Identify the preparation type.
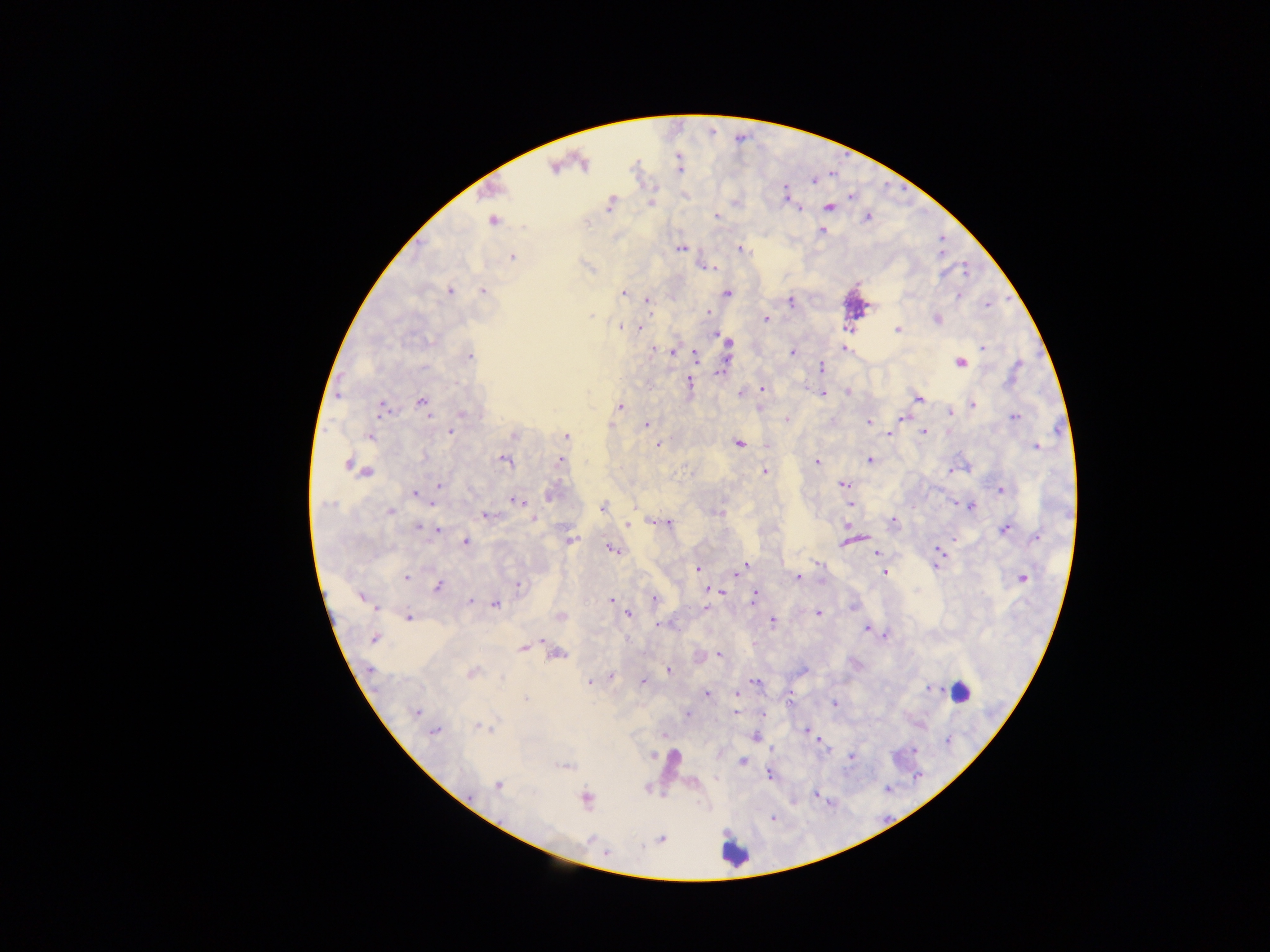
This is a thick smear.

Approximate centers as [x, y] in pixels. Plasmodium parasite locations: [554, 168], [813, 185], [784, 194], [614, 199], [651, 203], [828, 207], [796, 209], [718, 219], [492, 221], [587, 222], [821, 231], [739, 248], [680, 249], [512, 257], [716, 267], [964, 272], [945, 274], [940, 275], [482, 290], [450, 291], [623, 292], [727, 292], [958, 297], [647, 299], [790, 300], [988, 305], [708, 312], [592, 314], [938, 318], [765, 320], [622, 325], [640, 327], [897, 328], [845, 329], [721, 337], [729, 341], [845, 347], [983, 347], [657, 349], [792, 352], [694, 355], [471, 356], [960, 362], [821, 365], [1020, 365], [723, 368], [763, 388], [822, 392], [847, 392], [919, 399], [421, 403], [973, 403], [621, 406], [380, 412], [950, 412], [902, 416], [429, 417], [1014, 418], [868, 423], [609, 424], [646, 424], [450, 433], [891, 433], [925, 433], [512, 434], [369, 437], [565, 437], [739, 442], [658, 446], [1038, 446], [559, 458], [869, 460], [507, 462], [817, 462], [346, 465], [950, 470], [369, 471], [765, 471], [842, 485], [440, 486], [1003, 489], [416, 492], [512, 501], [517, 502], [636, 502], [849, 502], [972, 506], [602, 507], [391, 513], [484, 515], [533, 519], [670, 521], [894, 521], [627, 525], [418, 528], [440, 528], [1006, 528], [1037, 536], [861, 537], [956, 539], [465, 543], [571, 543], [844, 543], [613, 549], [940, 550], [876, 552], [746, 564], [819, 564], [696, 567], [941, 568], [736, 573], [884, 573], [407, 576], [797, 577], [1023, 578], [519, 585], [438, 586], [719, 592], [753, 596], [361, 598], [470, 599], [612, 599], [495, 606], [377, 609], [817, 613], [628, 614], [559, 616], [408, 617], [772, 621], [658, 623], [866, 629], [374, 640], [546, 640], [522, 648], [561, 654], [720, 654], [670, 670], [803, 670], [473, 673], [613, 677], [642, 681], [753, 681], [591, 682], [931, 689], [964, 691], [706, 693], [734, 695], [526, 699], [834, 703], [417, 711], [734, 711], [687, 715], [479, 728], [804, 731], [436, 734], [664, 736], [758, 736], [823, 745], [772, 749], [914, 749], [653, 756], [850, 758], [742, 762], [569, 765], [559, 766], [769, 775], [718, 778], [497, 787], [887, 791], [814, 792], [586, 799], [794, 802], [771, 820]. Leukocyte locations: [725, 851]. Photographed through a microscope with a mobile-phone camera. Image is 1270×952 pixels. Collected in Ghana. Single field of view.